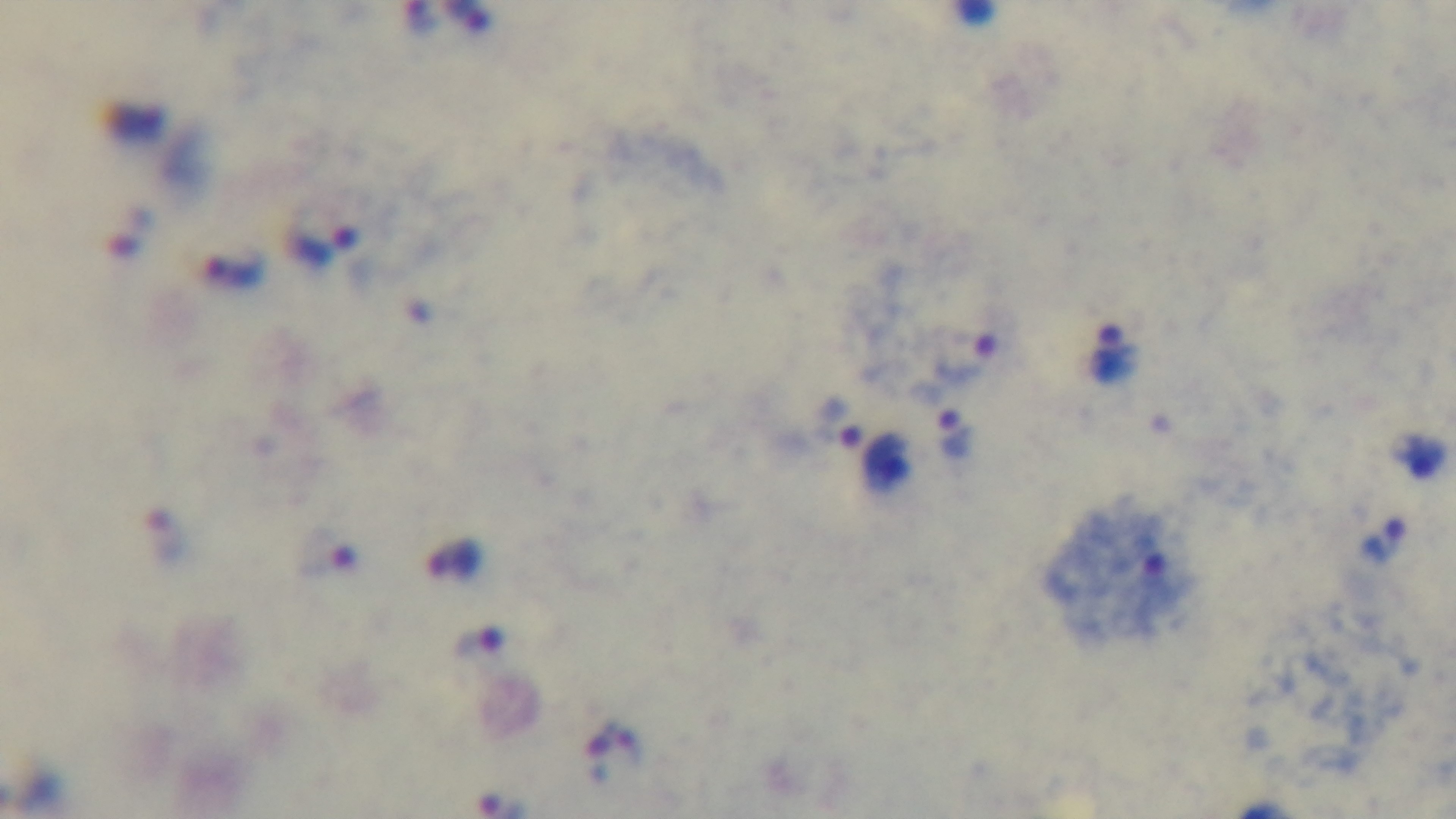
Summary:
  - Objective: 100x oil immersion
  - Stain: Giemsa
  - Field of view: one from the slide
  - Preparation: thick smear
  - Modality: light microscopy
  - Malaria status: infected
  - Capture: mounted 4K digital camera